Assess for malaria.
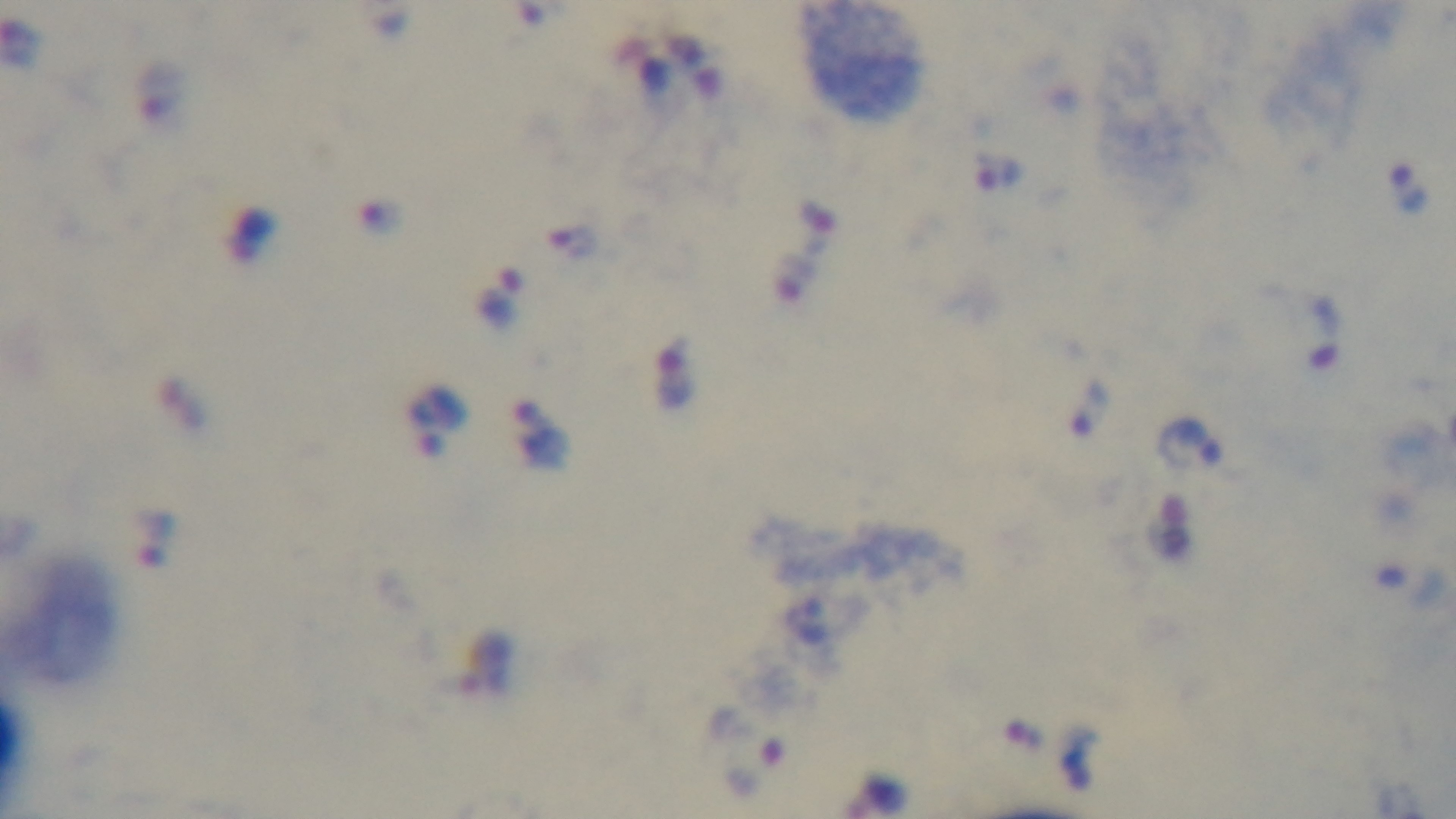
It is infected.

Summary:
  - Capture: mounted 4K digital camera
  - Field of view: single
  - Preparation: thick smear
  - Objective: 100x oil immersion
  - Modality: light microscopy
  - Stain: Giemsa